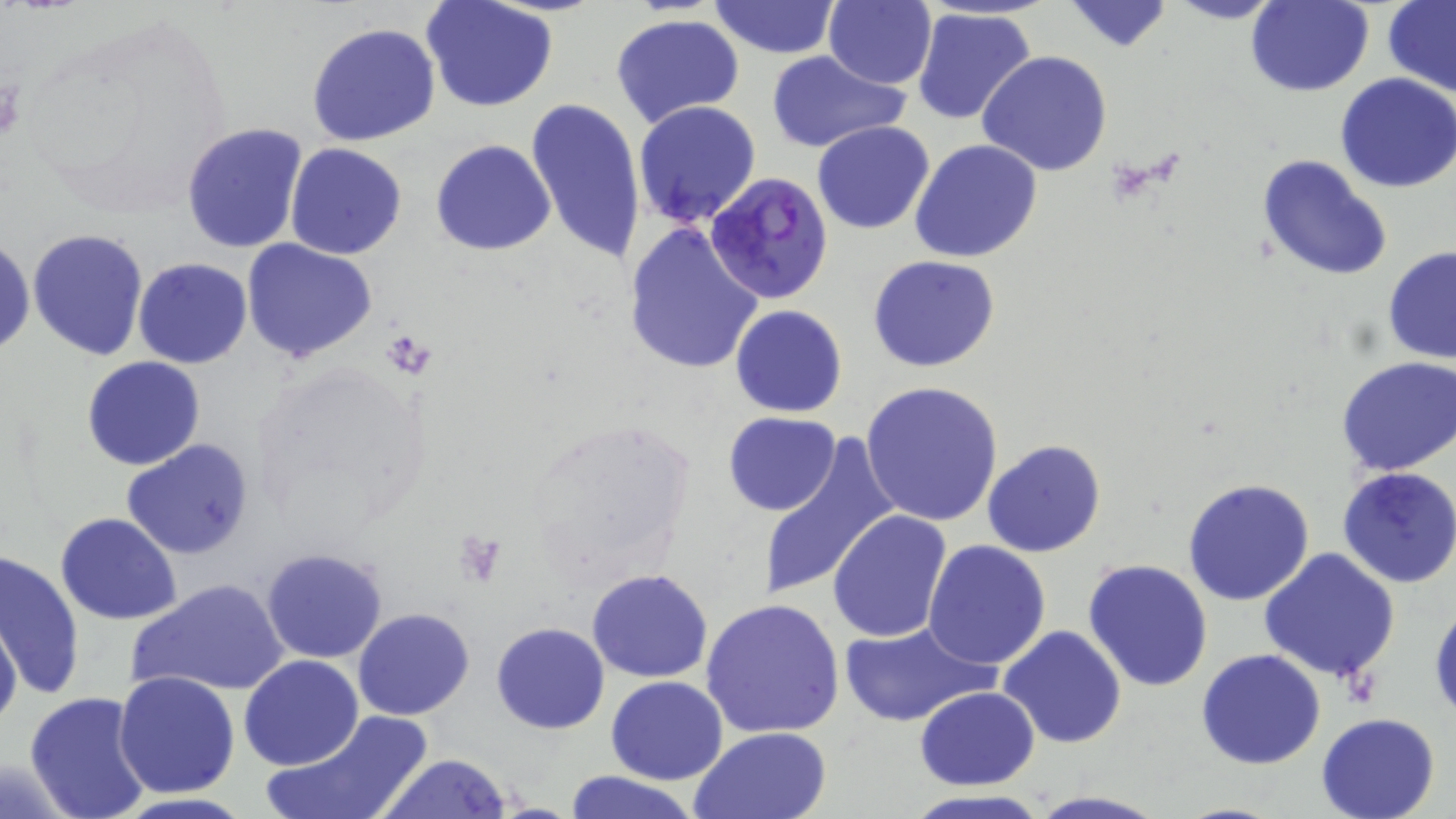

Summary:
  - Coordinate format: approximate bounding boxes as (x1, y1, x2, y2) in pixels
  - Uninfected red blood cell locations: (420, 0, 558, 113), (1166, 0, 1287, 24), (707, 1, 839, 60), (823, 1, 938, 88), (1061, 1, 1175, 53), (1244, 1, 1374, 97), (1382, 1, 1456, 97), (912, 8, 1038, 128), (611, 14, 745, 127), (304, 22, 444, 148), (766, 50, 908, 153), (978, 51, 1112, 176), (1335, 73, 1456, 193), (526, 98, 646, 269), (633, 101, 762, 228), (812, 120, 936, 235), (181, 123, 308, 253), (431, 138, 557, 256), (909, 140, 1043, 263), (285, 142, 409, 259), (1257, 154, 1393, 281), (622, 221, 764, 376), (27, 228, 149, 362), (0, 232, 35, 359), (241, 238, 377, 364), (1383, 246, 1456, 365), (867, 254, 1000, 373), (132, 258, 253, 369), (730, 303, 848, 418), (1334, 356, 1456, 475), (81, 357, 206, 471), (861, 380, 1005, 526), (724, 411, 841, 516), (757, 434, 902, 601), (121, 439, 256, 558), (982, 439, 1106, 557), (1336, 466, 1456, 589), (1183, 479, 1315, 606), (827, 512, 952, 644), (55, 513, 183, 623), (923, 540, 1052, 669), (260, 548, 389, 664), (1260, 548, 1401, 684), (0, 551, 84, 701), (1082, 559, 1213, 691), (587, 568, 712, 682), (129, 577, 290, 699), (1429, 598, 1456, 725), (700, 599, 847, 740), (352, 607, 475, 720), (0, 618, 22, 733), (838, 620, 996, 728), (491, 622, 609, 734), (997, 626, 1127, 750), (1197, 647, 1326, 769), (239, 656, 363, 770), (113, 670, 240, 798), (606, 674, 728, 784), (914, 687, 1041, 790), (23, 690, 155, 819), (262, 709, 437, 819), (1314, 713, 1440, 819), (687, 727, 833, 819), (375, 753, 514, 818), (0, 755, 85, 817), (564, 770, 700, 819), (895, 790, 1056, 819), (1025, 790, 1170, 819)
  - Platelet locations: (455, 535, 503, 585)
  - Plasmodium falciparum-infected red blood cell locations: (706, 172, 834, 304)
  - Slide-level diagnosis: Plasmodium falciparum
  - Modality: light microscopy
  - Preparation: thin blood film
  - Image size: 1456×819 pixels
  - Stain: May-Grünwald-Giemsa
  - Field of view: one of a larger specimen
  - Magnification: 1000x